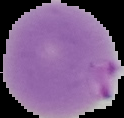

From a thin blood smear. The area outside the segmented cell region is set to black. Image is 124×118 pixels. Malaria status: parasitized.